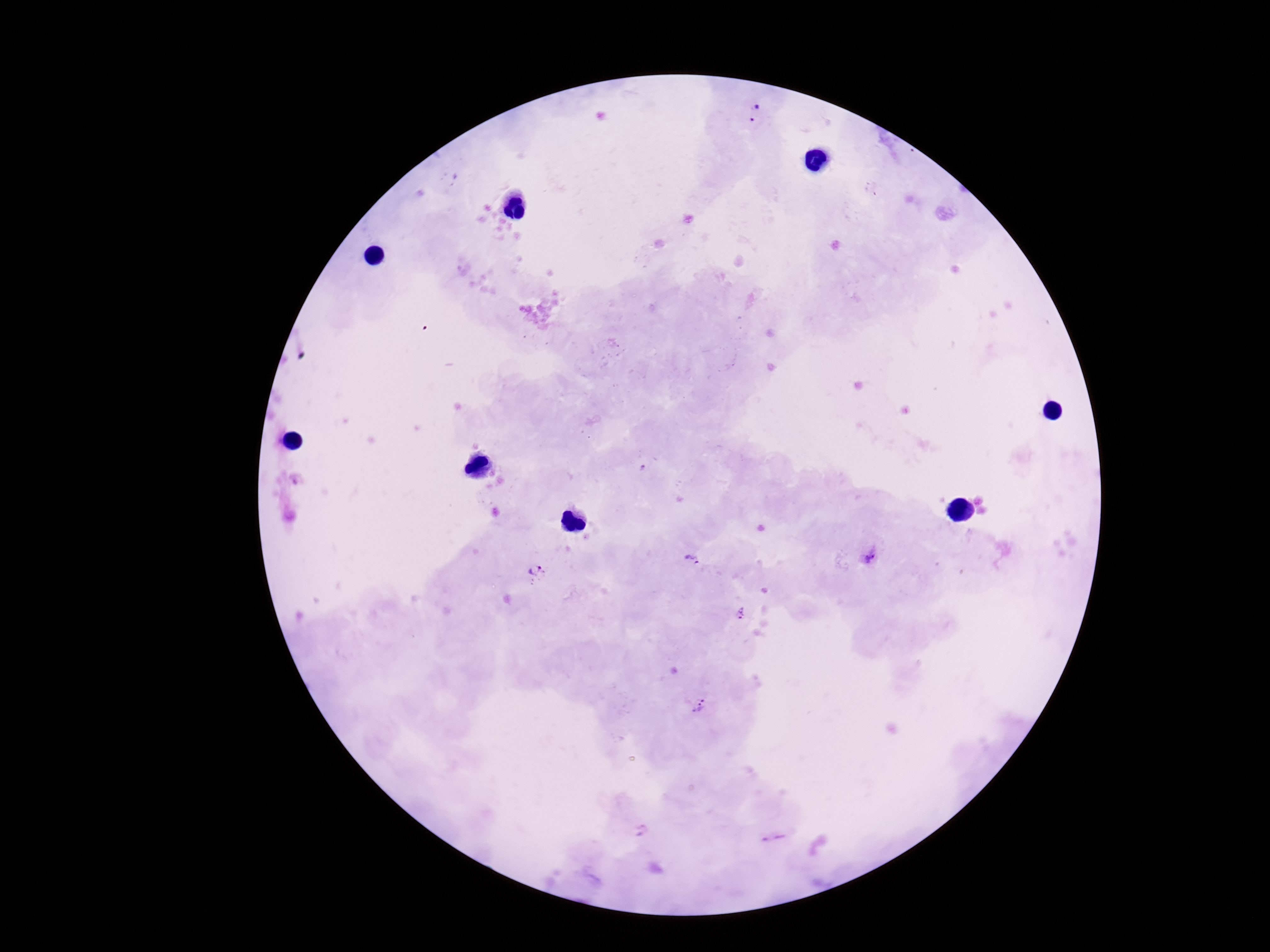
Approximate centers as [x, y] in pixels. Plasmodium parasite locations: [754, 113], [871, 557], [692, 560], [535, 571], [738, 613], [699, 705], [640, 831], [775, 836]. Giemsa-stained preparation. Thick blood smear. Patient malaria status: positive. Smartphone photograph taken through the microscope eyepiece. 100x magnification. One field from this slide. Image is 1270×952 pixels.